Identify the blood parasite species.
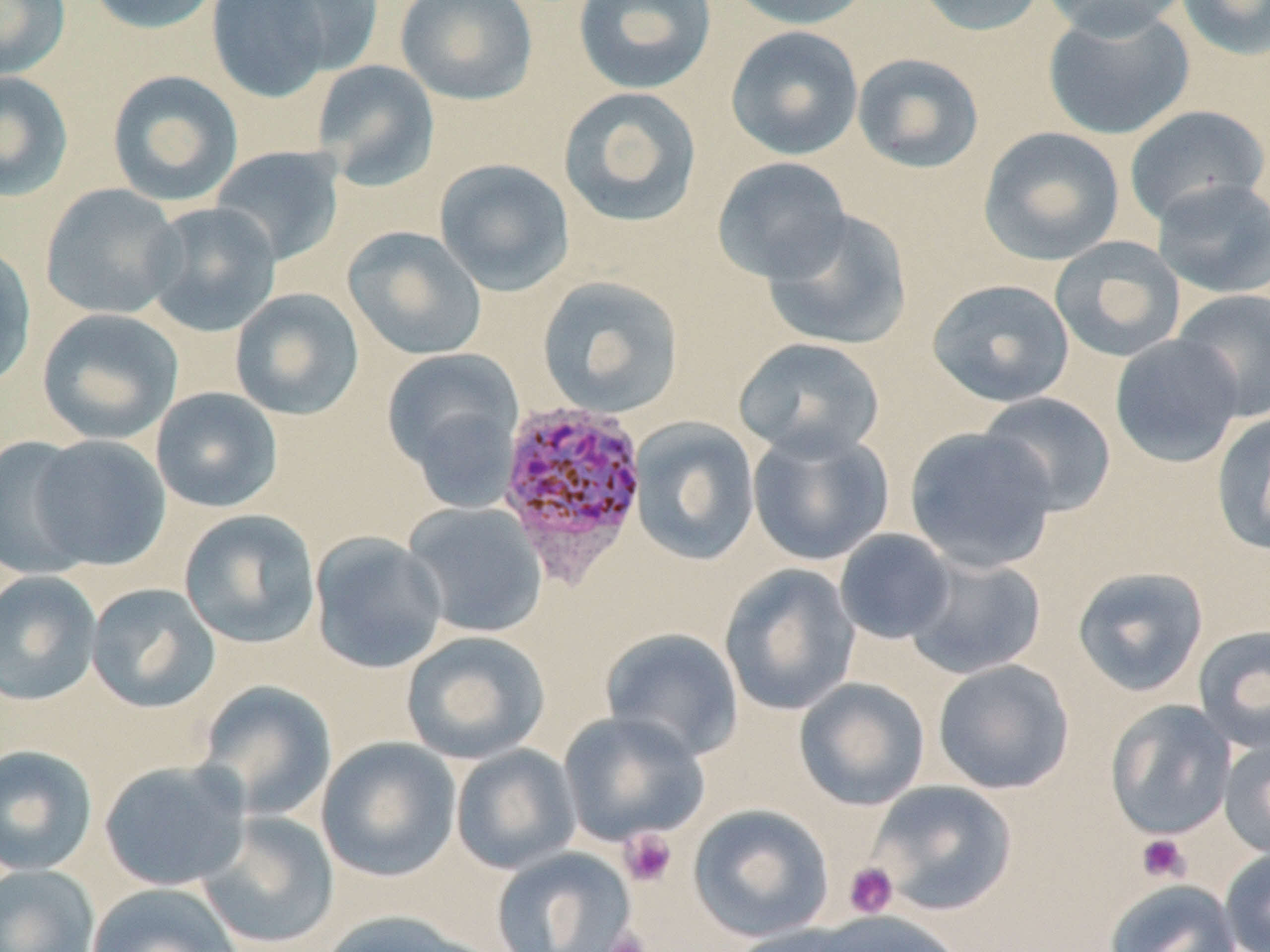

Plasmodium vivax.

Approximate bounding boxes as [x1, y1, x2, y2] in pixels. Uninfected red blood cell locations: [0, 0, 71, 81], [85, 0, 223, 35], [206, 0, 335, 103], [262, 0, 384, 75], [395, 0, 538, 106], [573, 0, 717, 95], [726, 0, 875, 30], [909, 0, 1048, 37], [1038, 0, 1191, 39], [1176, 0, 1270, 60], [1042, 5, 1195, 141], [725, 25, 864, 160], [851, 52, 985, 174], [311, 59, 440, 191], [106, 69, 244, 207], [0, 71, 74, 203], [557, 86, 703, 228], [1124, 104, 1269, 226], [978, 126, 1126, 266], [209, 145, 345, 267], [711, 156, 851, 285], [434, 157, 575, 296], [1152, 178, 1270, 299], [40, 183, 184, 320], [142, 202, 282, 337], [762, 209, 912, 351], [343, 226, 487, 361], [1049, 236, 1186, 364], [0, 242, 37, 392], [536, 275, 685, 419], [926, 278, 1075, 408], [229, 287, 364, 421], [1172, 289, 1270, 422], [36, 308, 184, 445], [1110, 334, 1244, 468], [733, 337, 886, 462], [381, 347, 525, 501], [150, 386, 283, 512], [977, 392, 1117, 518], [1211, 410, 1270, 557], [628, 417, 760, 566], [904, 425, 1059, 574], [747, 426, 894, 566], [29, 434, 171, 571], [0, 435, 96, 579], [402, 501, 547, 638], [178, 509, 321, 648], [834, 528, 956, 645], [308, 532, 449, 675], [903, 553, 1047, 680], [718, 563, 861, 716], [1072, 566, 1209, 697], [0, 570, 102, 707], [85, 582, 221, 715], [1192, 624, 1270, 753], [600, 626, 744, 761], [401, 630, 550, 765], [932, 659, 1075, 794], [794, 677, 930, 811], [195, 680, 338, 822], [1105, 699, 1237, 841], [557, 710, 709, 847], [316, 737, 462, 882], [1218, 737, 1270, 858], [0, 744, 99, 876], [450, 744, 581, 875], [99, 759, 251, 892], [868, 780, 1017, 916], [688, 803, 834, 942], [196, 811, 341, 950], [491, 846, 637, 952], [1220, 846, 1270, 952], [0, 863, 100, 952], [1103, 878, 1242, 952], [85, 882, 244, 952], [316, 908, 491, 952], [806, 910, 964, 952], [725, 922, 876, 952]. Platelet locations: [619, 828, 678, 887], [1136, 834, 1190, 883], [843, 862, 899, 919], [603, 928, 652, 952]. Plasmodium vivax-infected red blood cell locations: [495, 399, 650, 584]. Thin blood film. Light microscopy. Single field of view. May-Grünwald-Giemsa stain. Image is 1270×952 pixels. 1000x magnification.